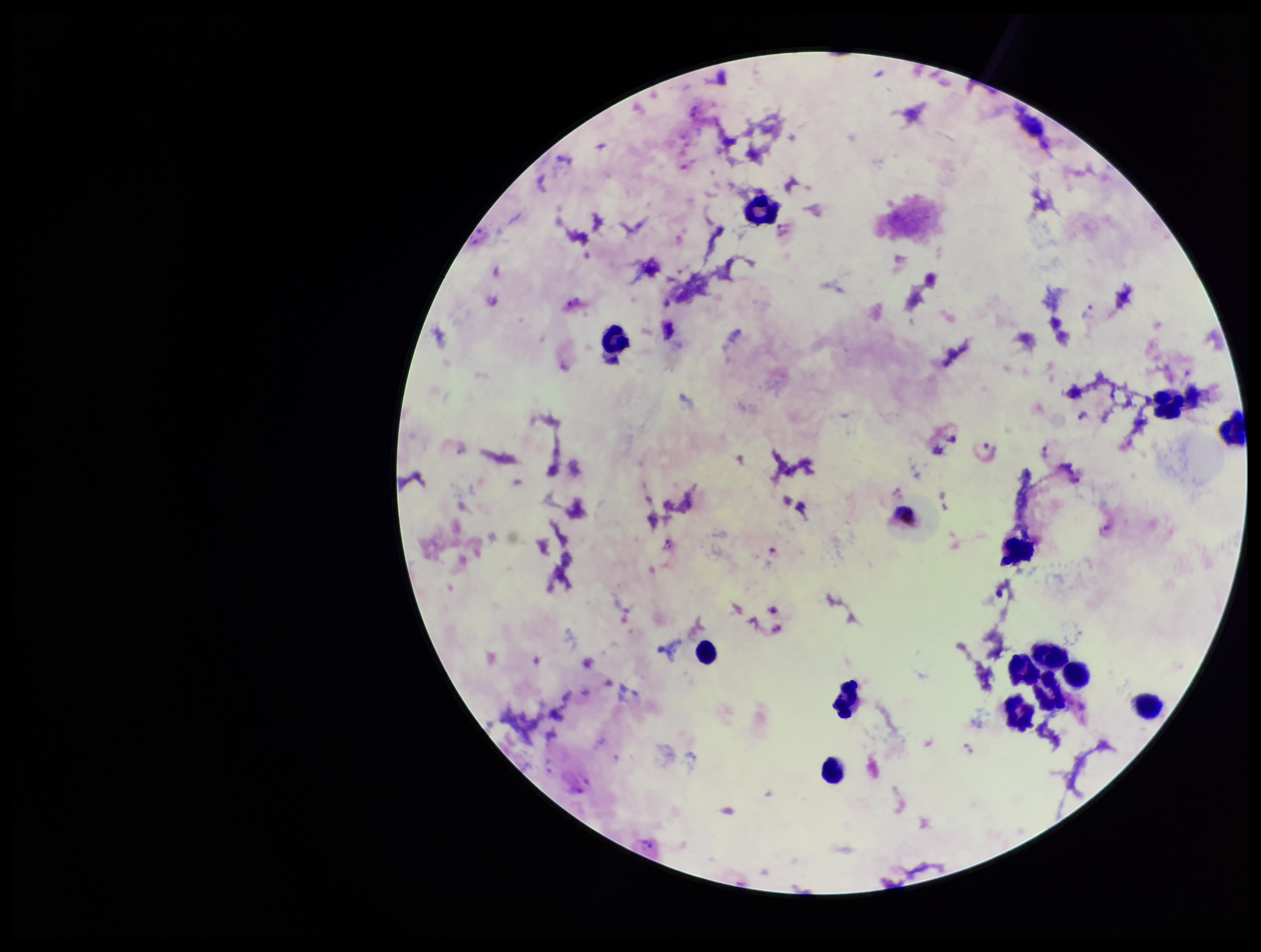
One field from this slide. Leukocyte count: 14. Plasmodium parasites: seen. Species reported for this patient: Plasmodium vivax. Stained with Giemsa. Preparation: thick. Smartphone photograph taken through the eyepiece of a microscope. Image is 1261×952 pixels. Patient malaria status: positive. Parasite count: 3.